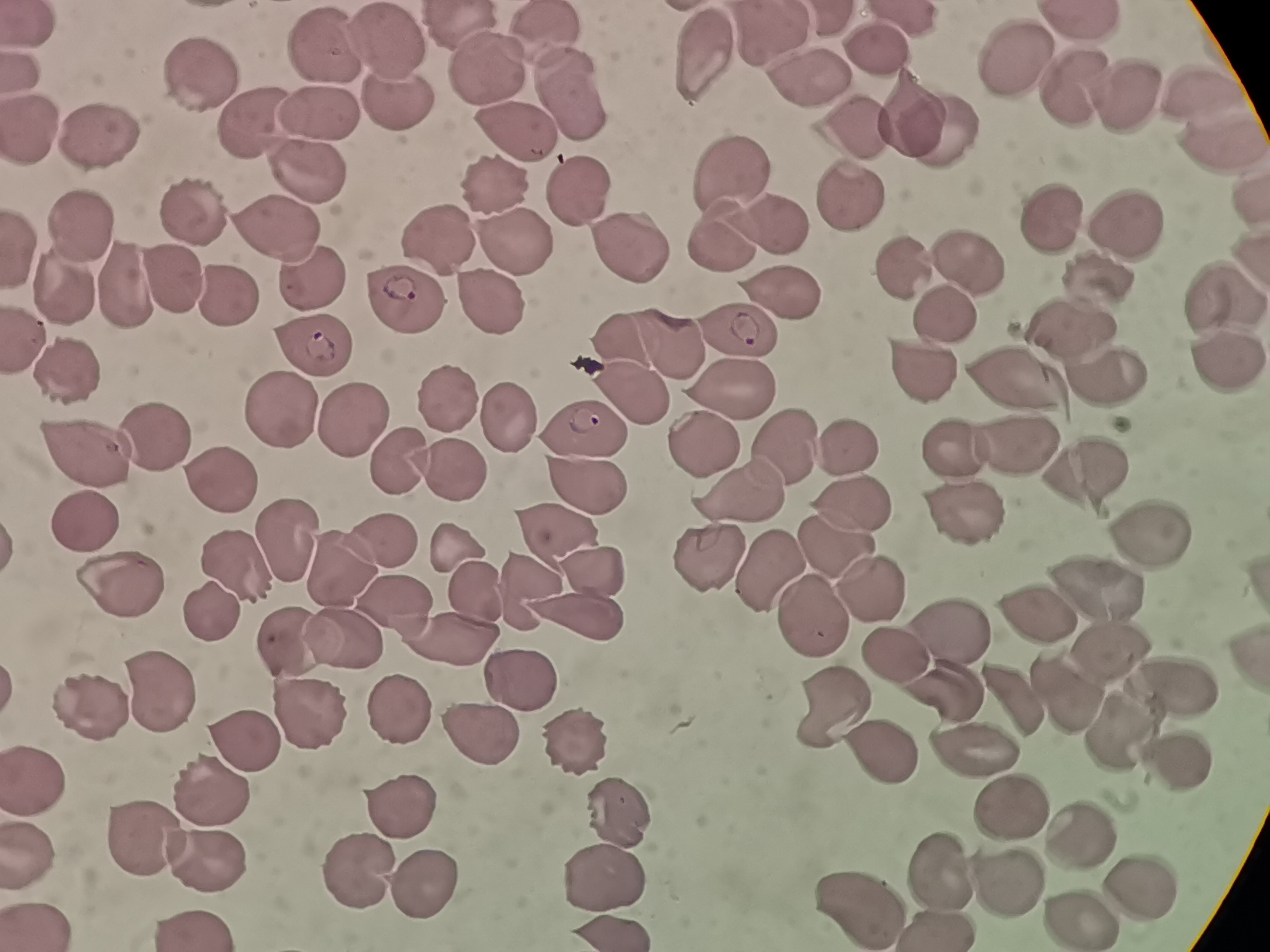

Approximate centers as (x, y) in pixels.
Summary:
  - Cell locations: (773, 28), (35, 30), (551, 39), (391, 40), (324, 44), (693, 49), (882, 50), (1012, 53), (23, 72), (489, 72), (193, 74), (805, 77), (1072, 86), (1200, 88), (1122, 95), (574, 97), (911, 109), (399, 111), (323, 115), (251, 122), (856, 123), (930, 126), (37, 127), (518, 127), (1221, 138), (106, 140), (312, 170), (734, 177), (491, 179), (581, 194), (850, 195), (1247, 203), (197, 211), (1048, 215), (86, 222), (279, 223), (1132, 224), (771, 229), (448, 233), (725, 238), (23, 242), (517, 246), (636, 252), (961, 267), (900, 273), (1107, 278), (121, 279), (316, 281), (170, 282), (67, 284), (1226, 292), (219, 293), (783, 293), (489, 301), (412, 304), (950, 316), (1074, 326), (741, 332), (30, 333), (617, 335), (668, 341), (312, 348), (1224, 359), (917, 364), (76, 371), (1014, 374), (1112, 379), (738, 388), (451, 395), (638, 395), (276, 407), (505, 415), (350, 416), (590, 426), (159, 437), (783, 441), (951, 441), (702, 444), (850, 445), (1021, 448), (92, 457), (403, 458), (451, 471), (1090, 475), (585, 487), (220, 488), (745, 490), (853, 502), (966, 514), (90, 524), (554, 529), (1151, 529), (282, 538), (387, 538), (836, 541), (455, 543), (709, 552), (337, 562), (591, 562), (233, 567), (771, 571), (873, 580), (118, 583), (1104, 585), (524, 589), (471, 591), (211, 606), (403, 606), (586, 609), (1035, 614), (816, 617), (946, 632), (462, 633), (349, 637), (294, 638), (1103, 649), (893, 651), (524, 673), (1173, 681), (954, 686), (155, 694), (1065, 694), (839, 700), (92, 702), (1010, 703), (400, 704), (308, 709), (1124, 726), (483, 738), (575, 741), (253, 747), (872, 750), (975, 754), (1177, 759), (32, 774), (211, 789), (1010, 803), (402, 805), (622, 813), (1077, 833), (150, 837), (33, 852), (216, 857), (933, 866), (605, 872), (358, 874), (424, 879), (1141, 880), (1004, 885), (863, 900), (1077, 917), (942, 924), (42, 925), (198, 925)
  - Preparation: thin blood film
  - Field of view: single
  - Stain: Giemsa
  - Image size: 1270×952 pixels
  - Capture: smartphone through the microscope eyepiece